State the preparation type.
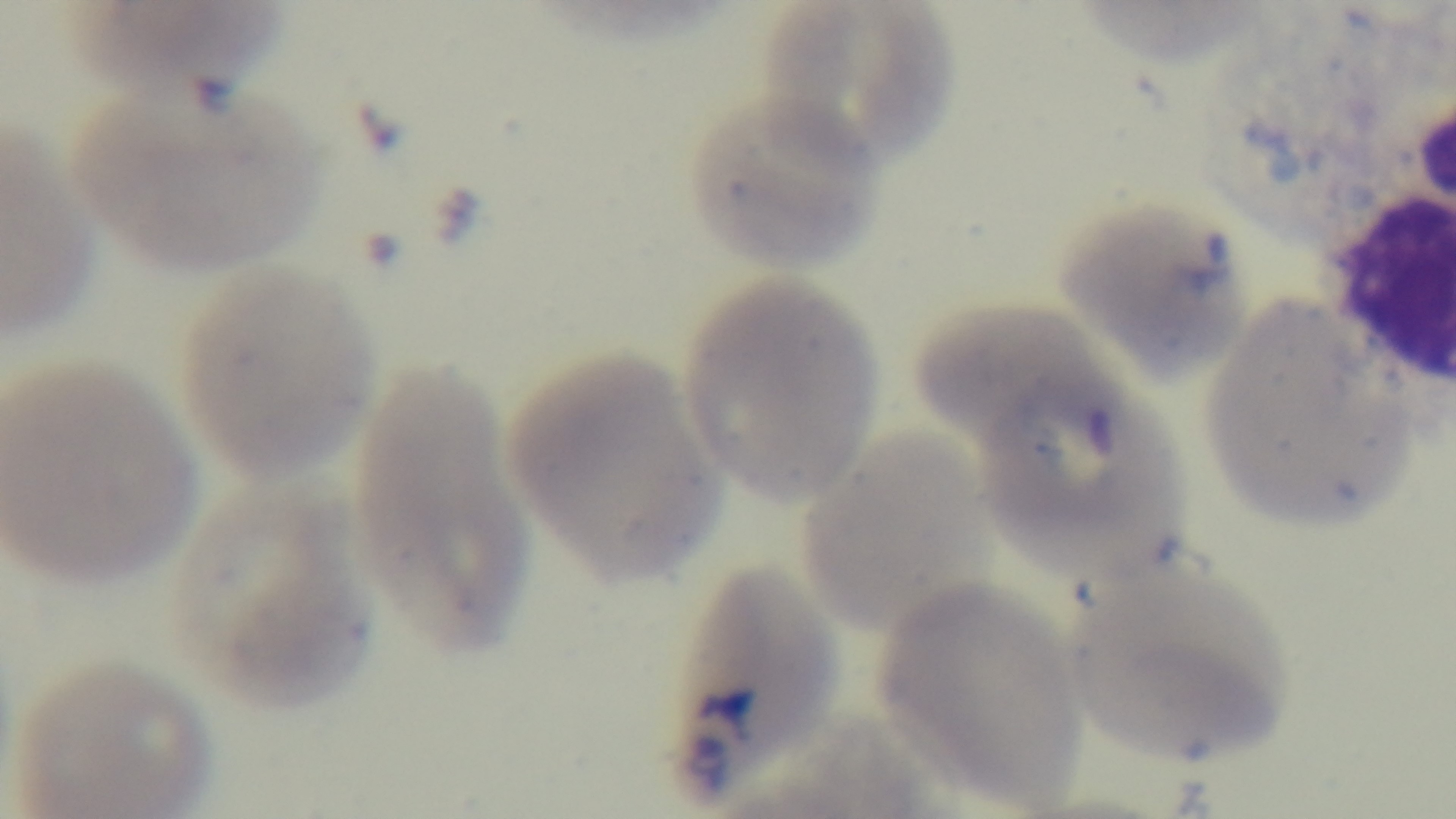
It is a thin blood film.

{
  "objective": "100x oil immersion",
  "capture": "mounted 4K digital camera",
  "modality": "light microscopy",
  "malaria_status": "positive",
  "stain": "Giemsa",
  "field_of_view": "one from the slide"
}